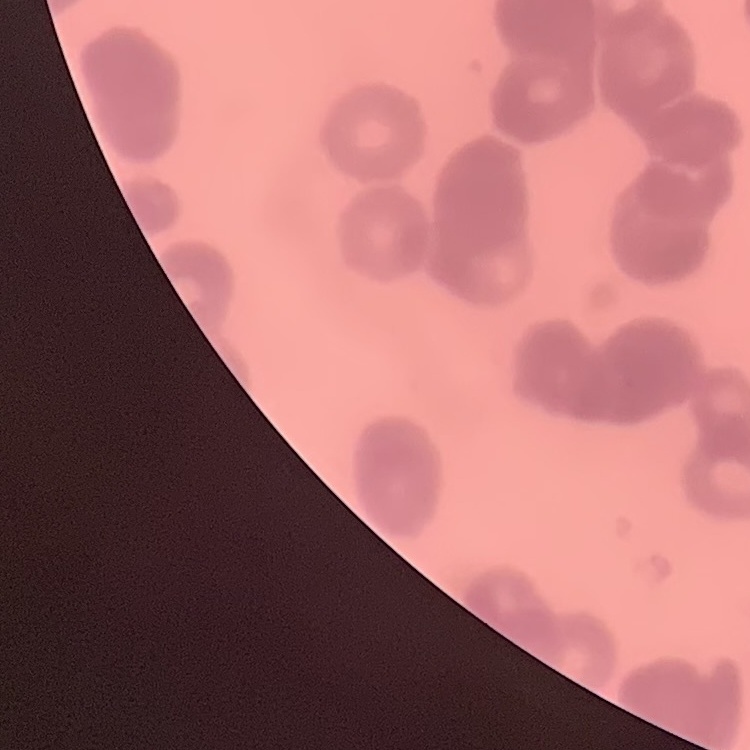
The red blood cells show rouleaux formation. One tile cut from a larger photomicrograph. Thin blood smear. Stained with either Field's or Giemsa.